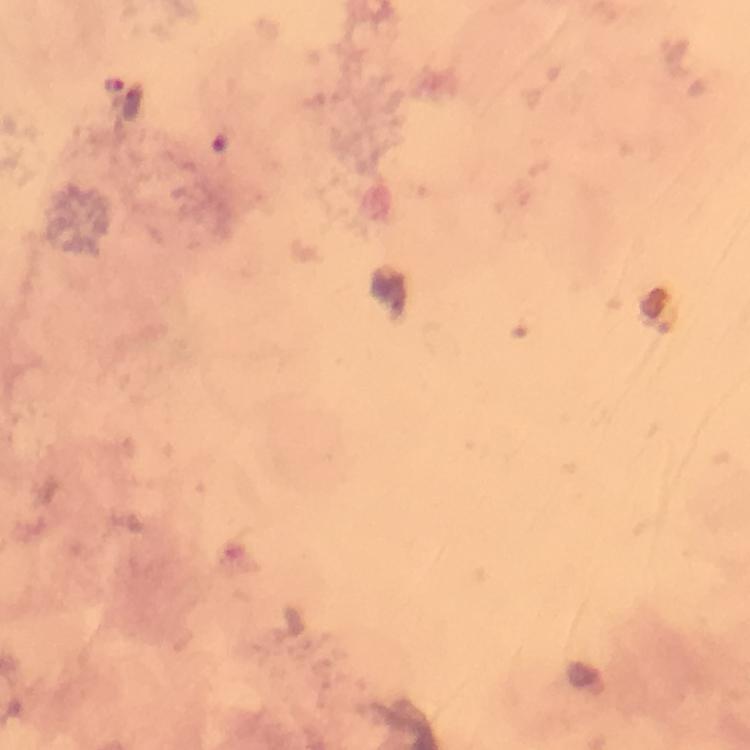

Approximate centers as (x, y) in pixels. Malaria parasite locations: (114, 85). Photographed with a smartphone mounted on the microscope. Cropped region of a single field of view. Thick smear. Immersion oil applied. Image is 750×750 pixels. Giemsa-stained preparation. At 100x magnification. From a diagnostic examination for malaria.